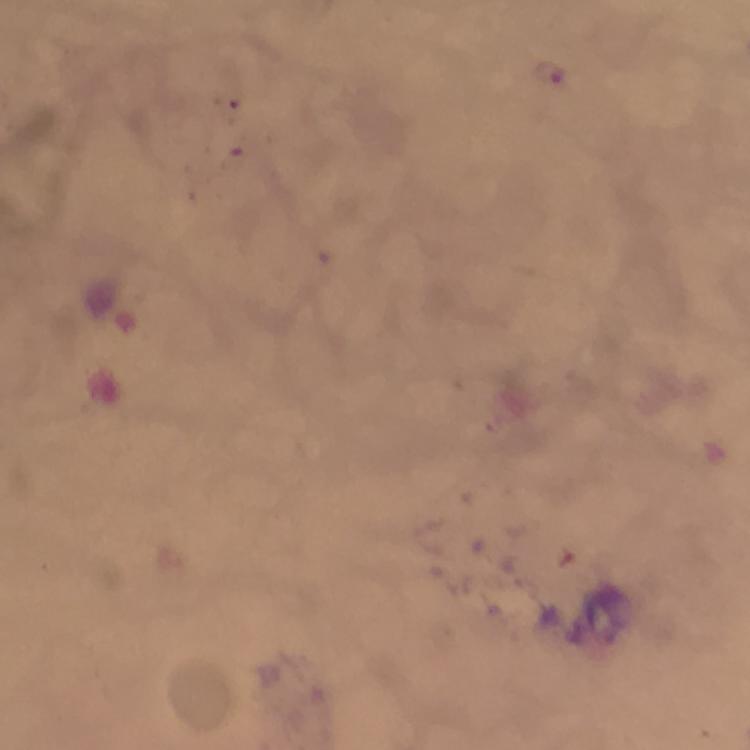

cropped from = a single field of view
capture = smartphone photograph through a microscope
magnification = 100x
immersion oil = applied
malaria parasite locations = approximate centers as (x, y) in pixels: (552, 74)
context = from a diagnostic examination for malaria
image size = 750×750 pixels
stain = Giemsa
preparation = thick smear